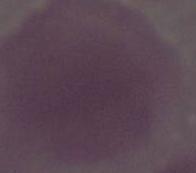
identification = red blood cell
modality = micrograph
magnification = 1000x